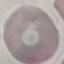

Summary:
  - Malaria status: uninfected
  - Preparation: thin smear
  - Stain: Giemsa
  - Capture: smartphone through the microscope eyepiece
  - Image type: cell patch, automatically extracted from a larger field of view and resized to 64 × 64 pixels